Report the malaria status of this cell.
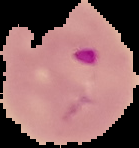
It is parasitized.

Summary:
  - Image size: 139×148 pixels
  - Image type: segmented cell region on a black background
  - Preparation: thin blood film